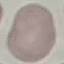

Summary:
  - Result: no malaria parasites detected
  - Stain: Giemsa
  - Image type: automatically extracted cell patch, resized to 64 × 64 pixels
  - Capture: smartphone camera at the microscope eyepiece
  - Preparation: thin blood smear